Classify this cell by malaria status.
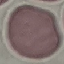
It is uninfected.

image type = cell patch, automatically extracted from a larger field of view and resized to 64 × 64 pixels
preparation = thin blood film
stain = Giemsa
capture = smartphone camera at the microscope eyepiece